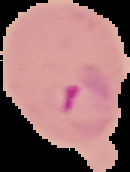

image_type: cell region segmented out of the field of view; surrounding area masked to black
preparation: thin blood smear
image_size: 130×172 pixels
result: Plasmodium parasites identified